Classify this cell by malaria status.
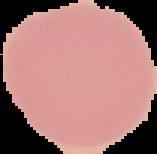

It is uninfected.

Summary:
  - Preparation: thin blood film
  - Image type: segmented cell region on a black background
  - Image size: 157×154 pixels